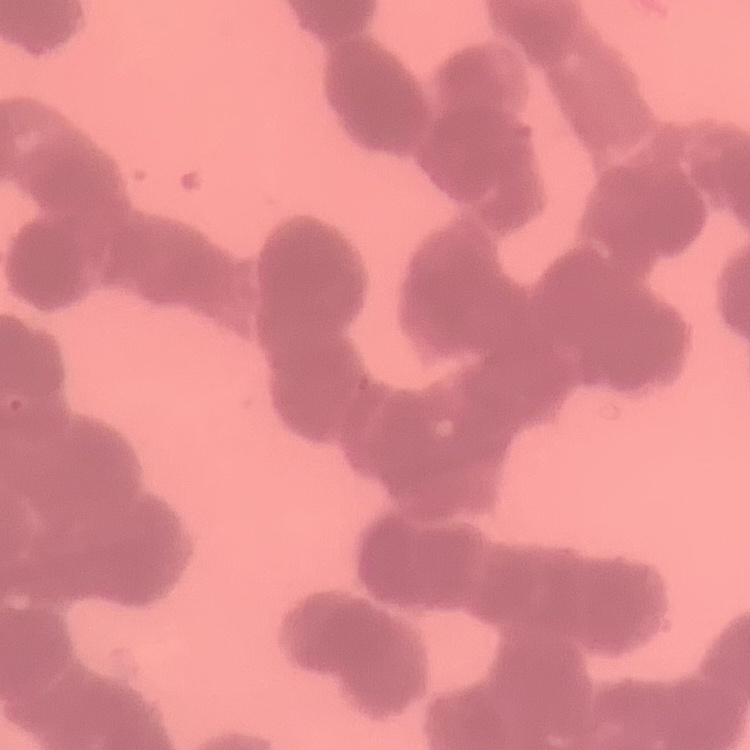

red blood cell morphology = rouleaux formation
preparation = thin blood smear
image type = one tile cut from a larger photomicrograph
stain = Field's or Giemsa